Classify this cell by malaria status.
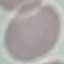
Uninfected.

Giemsa stain. Acquired by smartphone through the microscope eyepiece. Automatically extracted cell patch, resized to 64 × 64 pixels. Thin blood smear.